Assess for Plasmodium parasites.
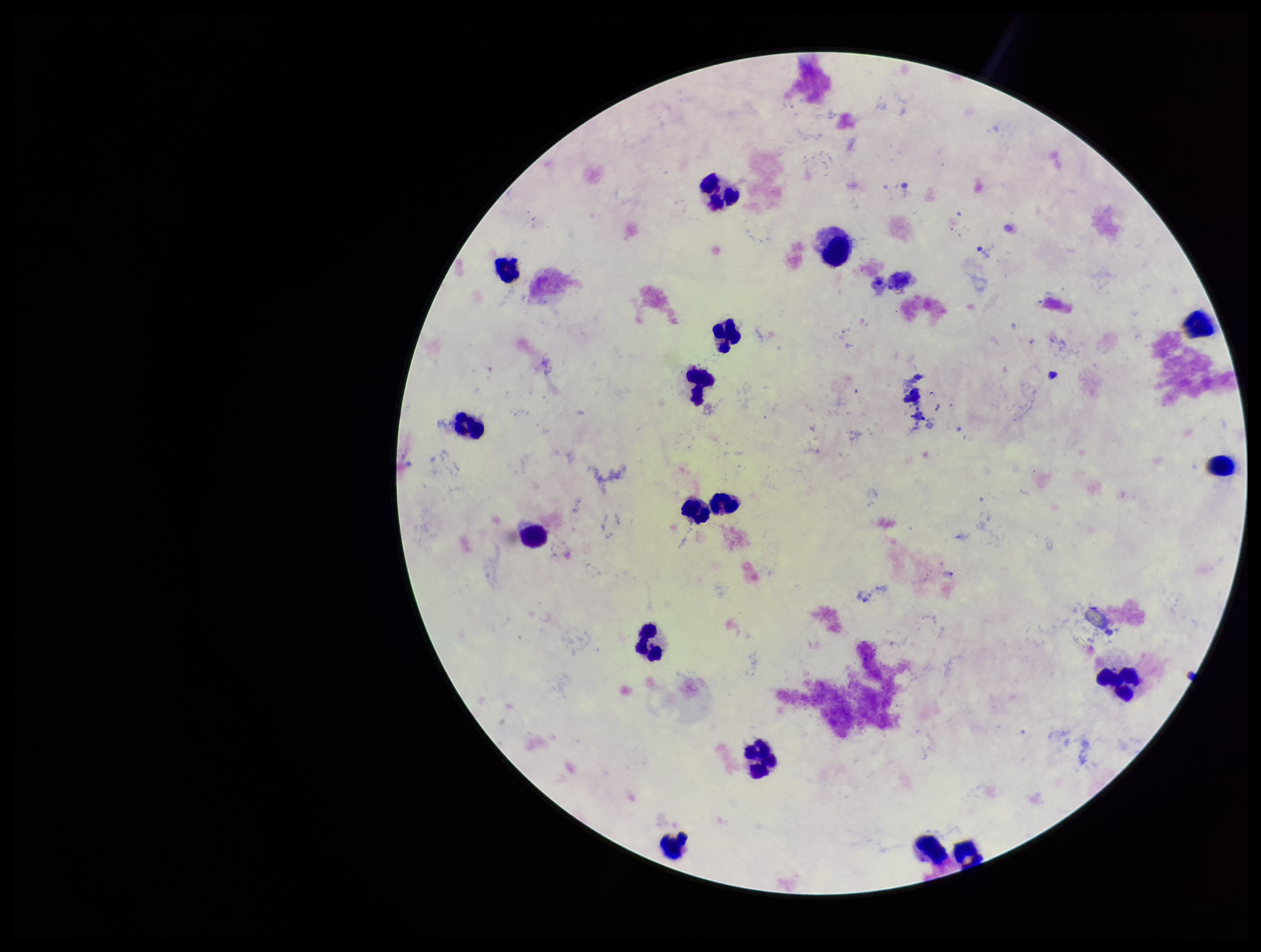

Seen.

{
  "field_of_view": "single",
  "image_size": "1261×952 pixels",
  "preparation": "thick blood smear",
  "stain": "Giemsa",
  "leukocyte_count": 17,
  "patient_malaria_status": "infected",
  "capture": "smartphone photograph through the microscope eyepiece",
  "parasite_count": 1,
  "species_reported_for_this_patient": "Plasmodium vivax"
}